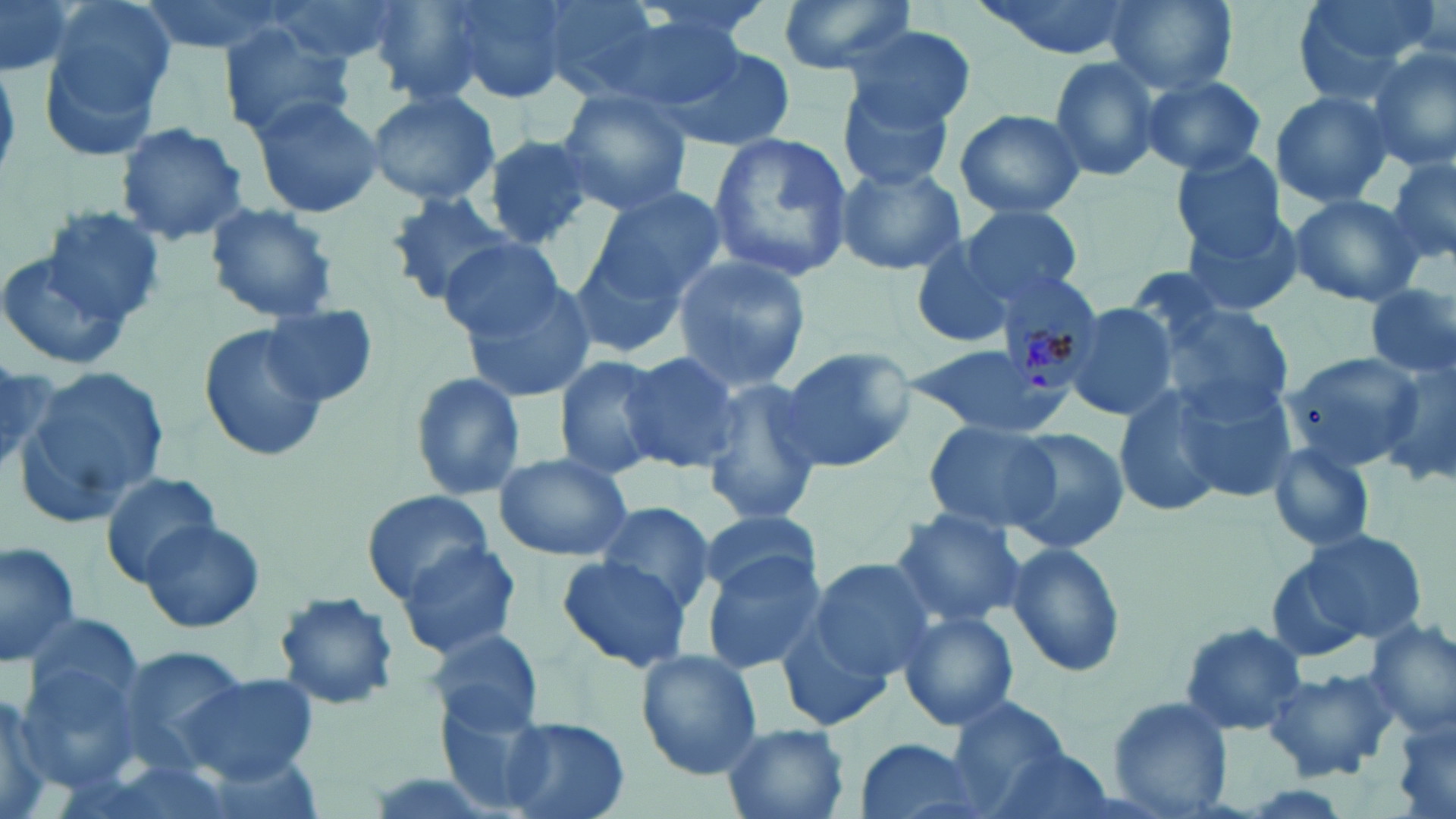
Approximate bounding boxes as (x1, y1, x2, y2) in pixels. Uninfected red blood cell locations: (0, 0, 79, 79), (132, 0, 300, 57), (265, 0, 405, 69), (441, 0, 575, 104), (531, 0, 673, 102), (622, 0, 779, 53), (772, 0, 921, 78), (974, 0, 1135, 59), (1105, 0, 1236, 95), (1291, 0, 1442, 103), (366, 1, 488, 101), (34, 3, 173, 157), (843, 25, 977, 130), (219, 28, 356, 142), (655, 41, 796, 152), (1365, 44, 1456, 172), (1047, 55, 1165, 181), (1139, 74, 1268, 176), (841, 83, 957, 191), (364, 89, 501, 205), (555, 89, 695, 215), (1269, 90, 1396, 207), (251, 94, 383, 220), (954, 108, 1087, 220), (114, 123, 249, 245), (708, 131, 854, 284), (480, 136, 600, 250), (1385, 150, 1456, 270), (1171, 151, 1289, 261), (834, 163, 964, 275), (588, 186, 727, 306), (383, 190, 519, 309), (1287, 193, 1425, 307), (204, 201, 339, 322), (960, 205, 1084, 305), (1178, 207, 1308, 318), (42, 208, 166, 325), (909, 230, 1027, 349), (437, 236, 564, 340), (0, 238, 142, 368), (568, 244, 690, 360), (670, 255, 811, 390), (460, 276, 596, 404), (1364, 285, 1456, 384), (1148, 291, 1300, 425), (1058, 302, 1178, 423), (260, 305, 379, 408), (198, 323, 329, 463), (899, 345, 1070, 440), (775, 346, 916, 470), (618, 352, 739, 470), (552, 353, 666, 479), (1377, 357, 1456, 488), (17, 364, 170, 526), (0, 368, 61, 474), (407, 370, 525, 502), (1173, 374, 1300, 502), (699, 378, 823, 528), (1111, 381, 1231, 521), (921, 420, 1060, 533), (1003, 427, 1128, 553), (1264, 440, 1380, 555), (908, 442, 1049, 612), (495, 453, 632, 561), (98, 472, 225, 583), (363, 489, 494, 600), (593, 502, 720, 612), (888, 507, 1029, 629), (695, 509, 825, 598), (137, 517, 266, 635), (1272, 526, 1428, 655), (0, 537, 82, 667), (1003, 539, 1127, 679), (396, 542, 523, 659), (698, 552, 829, 675), (556, 555, 693, 672), (809, 556, 941, 679), (272, 590, 401, 712), (898, 610, 1018, 731), (775, 616, 896, 734), (1363, 618, 1455, 738), (1177, 620, 1310, 737), (424, 628, 547, 734), (635, 649, 764, 778), (1262, 665, 1404, 782), (177, 675, 320, 784), (0, 682, 65, 819), (437, 694, 552, 812), (1104, 696, 1236, 817), (944, 697, 1072, 812), (1386, 707, 1456, 819), (501, 718, 629, 819), (722, 723, 851, 819), (851, 736, 990, 819), (982, 744, 1119, 819). Plasmodium malariae-infected red blood cell locations: (994, 263, 1104, 387). Slide-level diagnosis: Plasmodium malariae. Single field of view. May-Grünwald-Giemsa stain. 1000x magnification. Image is 1456×819 pixels. Optical microscopy. Thin blood smear.